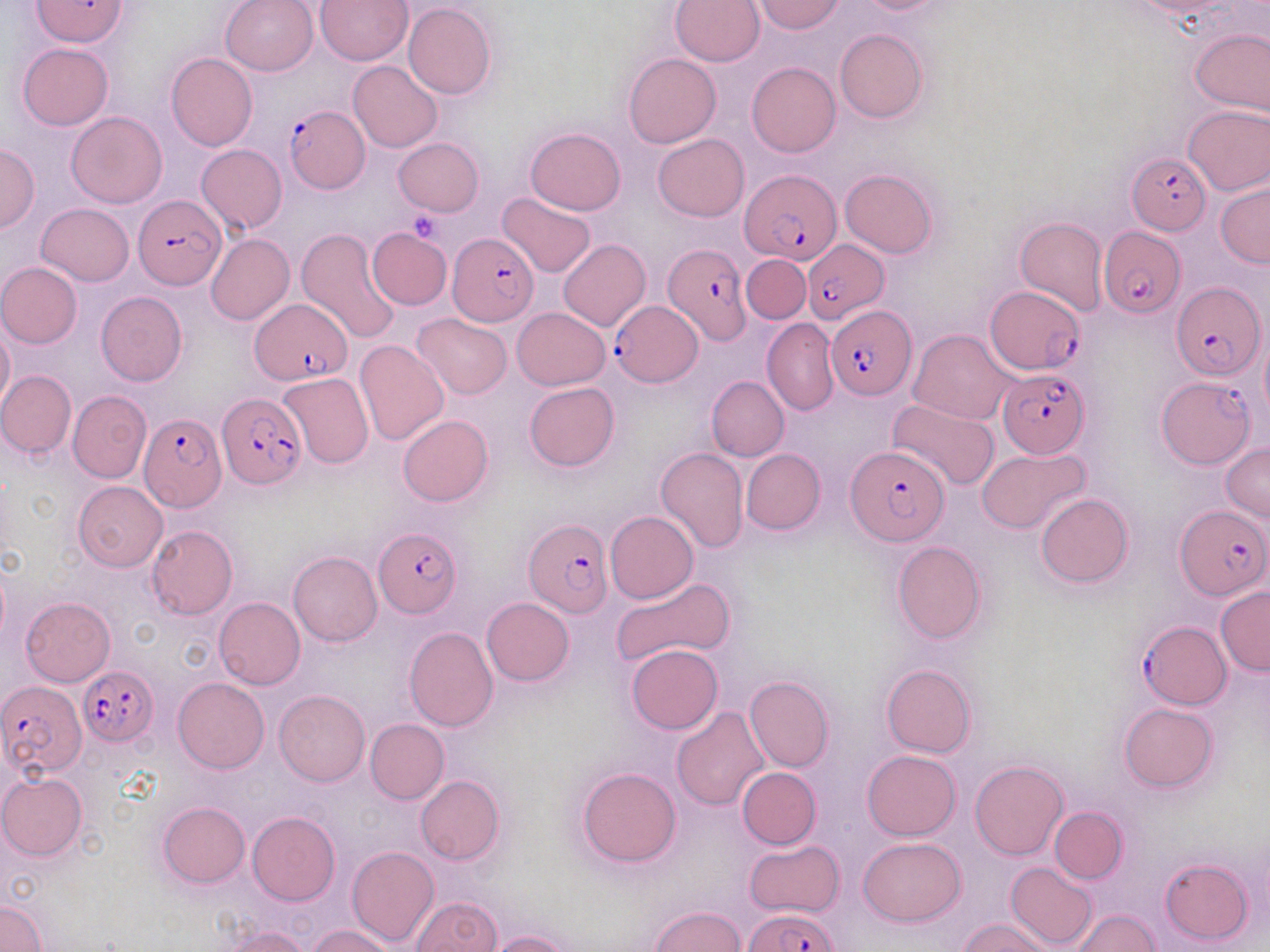
Approximate bounding boxes as (x1, y1, x2, y2) in pixels. Uninfected red blood cell locations (subset): (220, 0, 319, 75), (316, 0, 413, 65), (753, 0, 846, 34), (850, 0, 951, 15), (670, 1, 764, 67), (403, 3, 495, 100), (1190, 26, 1270, 117), (834, 29, 928, 123), (18, 43, 112, 131), (165, 52, 258, 150), (624, 53, 720, 148), (348, 60, 443, 152), (746, 62, 840, 156), (1184, 105, 1270, 194), (66, 111, 167, 209), (525, 127, 626, 215), (653, 134, 749, 221), (393, 138, 484, 216), (0, 143, 40, 233), (196, 143, 287, 234), (840, 169, 937, 258), (1215, 182, 1269, 267), (497, 191, 596, 277), (37, 202, 134, 286), (1015, 216, 1108, 315), (296, 228, 400, 345), (206, 233, 294, 326), (559, 238, 651, 331), (741, 255, 809, 324), (0, 262, 82, 348), (96, 291, 187, 386), (511, 308, 609, 390), (413, 313, 513, 400), (762, 319, 839, 416), (0, 321, 14, 410), (908, 329, 1017, 425), (355, 339, 449, 446), (0, 371, 76, 458), (278, 372, 374, 468), (707, 376, 789, 461), (525, 381, 619, 471), (68, 390, 151, 483), (887, 398, 1000, 491), (398, 415, 493, 506), (1220, 442, 1270, 522), (655, 447, 748, 553), (978, 447, 1091, 534), (741, 448, 825, 534), (74, 482, 168, 572), (1037, 493, 1132, 587), (606, 511, 698, 603), (146, 525, 237, 619), (892, 541, 987, 643), (289, 551, 383, 647), (611, 576, 735, 666), (1215, 587, 1269, 676), (20, 597, 115, 686), (213, 597, 304, 689), (481, 597, 574, 686), (404, 627, 498, 731), (626, 645, 724, 733), (881, 664, 976, 758), (744, 676, 834, 772), (173, 678, 269, 773), (274, 689, 369, 786), (1120, 703, 1218, 791), (672, 706, 770, 810), (366, 718, 449, 804), (863, 750, 960, 840), (970, 760, 1068, 860), (577, 767, 682, 867), (737, 768, 822, 848), (1, 772, 87, 860), (415, 776, 505, 865), (157, 802, 249, 887), (1050, 806, 1127, 883), (248, 811, 340, 906), (858, 837, 967, 927), (743, 840, 846, 917), (346, 846, 439, 947), (1161, 859, 1253, 945), (1006, 861, 1097, 950), (411, 896, 501, 951), (0, 899, 46, 951), (650, 905, 746, 952), (1071, 908, 1162, 950), (958, 918, 1056, 952), (308, 925, 395, 952), (218, 926, 313, 952), (486, 930, 577, 952). Plasmodium falciparum-infected red blood cell locations (subset): (284, 105, 369, 193), (1128, 151, 1211, 234), (741, 168, 842, 265), (134, 196, 226, 290), (1097, 227, 1185, 318), (448, 229, 537, 326), (803, 240, 889, 321), (662, 243, 749, 343), (1170, 281, 1265, 381), (984, 286, 1086, 375), (250, 296, 353, 384), (613, 301, 702, 385), (829, 307, 915, 399), (999, 369, 1092, 457), (1156, 376, 1257, 468), (216, 393, 306, 490), (138, 412, 226, 512), (846, 443, 950, 547), (1176, 504, 1268, 601), (523, 518, 612, 617), (374, 527, 462, 619), (1138, 620, 1230, 710), (79, 665, 159, 746), (0, 680, 86, 779), (745, 907, 838, 951). Platelet locations: (406, 208, 444, 244). Slide-level diagnosis: Plasmodium falciparum. Captured at 1000x magnification. Thin blood smear. Optical microscopy. Image is 1270×952 pixels. May-Grünwald-Giemsa-stained preparation. Single field of view.